Report the malaria status of this cell.
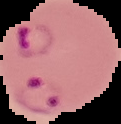
Parasitized.

Segmented cell region on a black background. From a thin blood smear. Image is 121×124 pixels.